Point out each Plasmodium parasite.
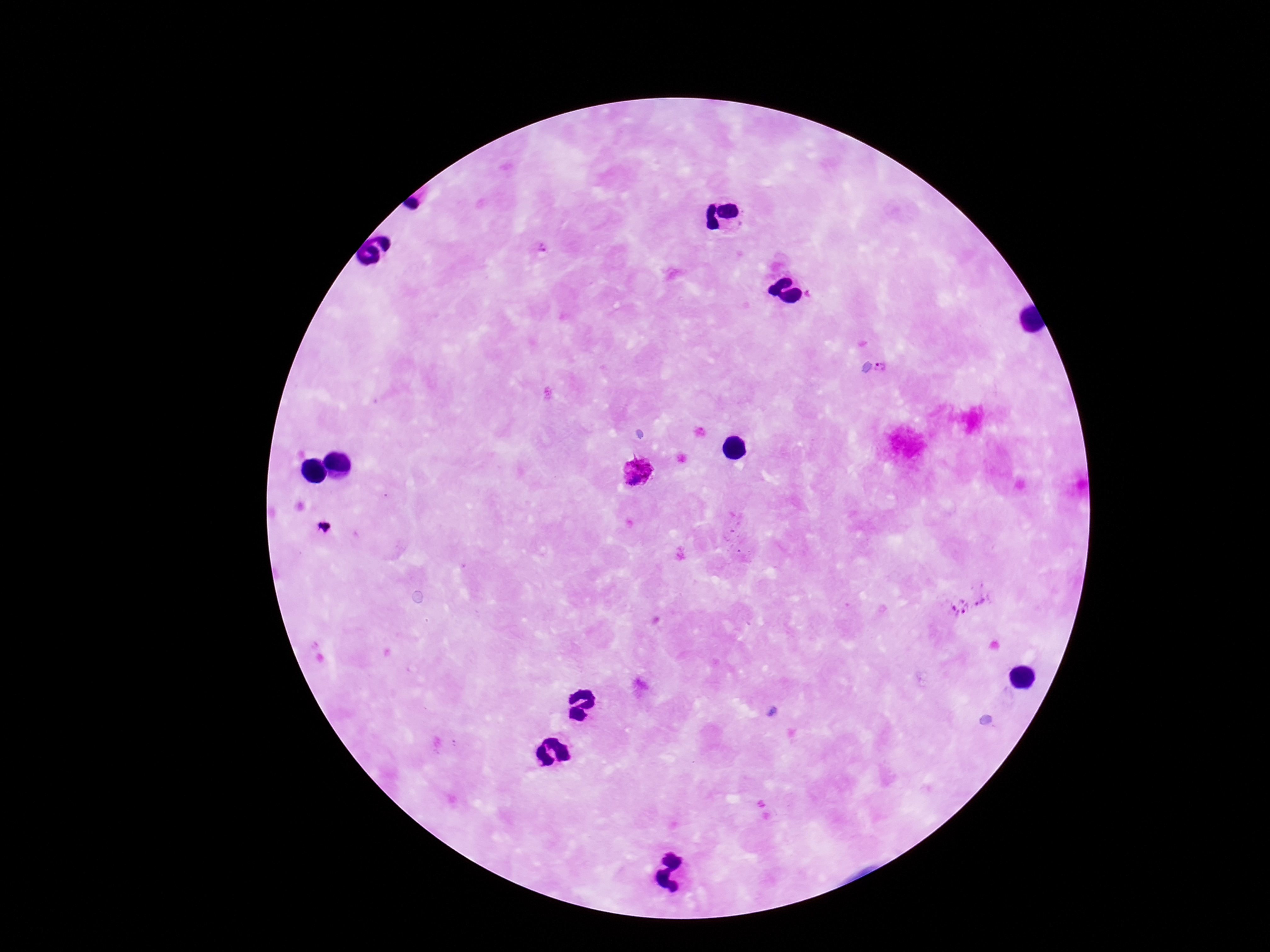
Approximate centers as [x, y] in pixels.
Plasmodium parasites: [541, 251], [882, 368], [637, 470], [320, 528], [973, 602].

Summary:
  - Image size: 1270×952 pixels
  - Patient malaria status: positive
  - Stain: Giemsa
  - Field of view: single
  - Preparation: thick blood smear
  - Magnification: 100x
  - Capture: smartphone camera through the microscope eyepiece